Assess this cell for malaria.
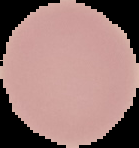
Uninfected.

From a thin blood film. Image is 139×148 pixels. Segmented cell region on a black background.